Assess this cell for malaria.
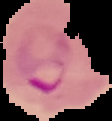
Parasitized.

From a thin blood smear. Image is 112×121 pixels. The area outside the segmented cell region is set to black.